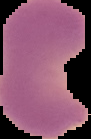 Result: Plasmodium parasites detected. Image is 91×139 pixels. From a thin blood film. Segmented cell region on a black background.